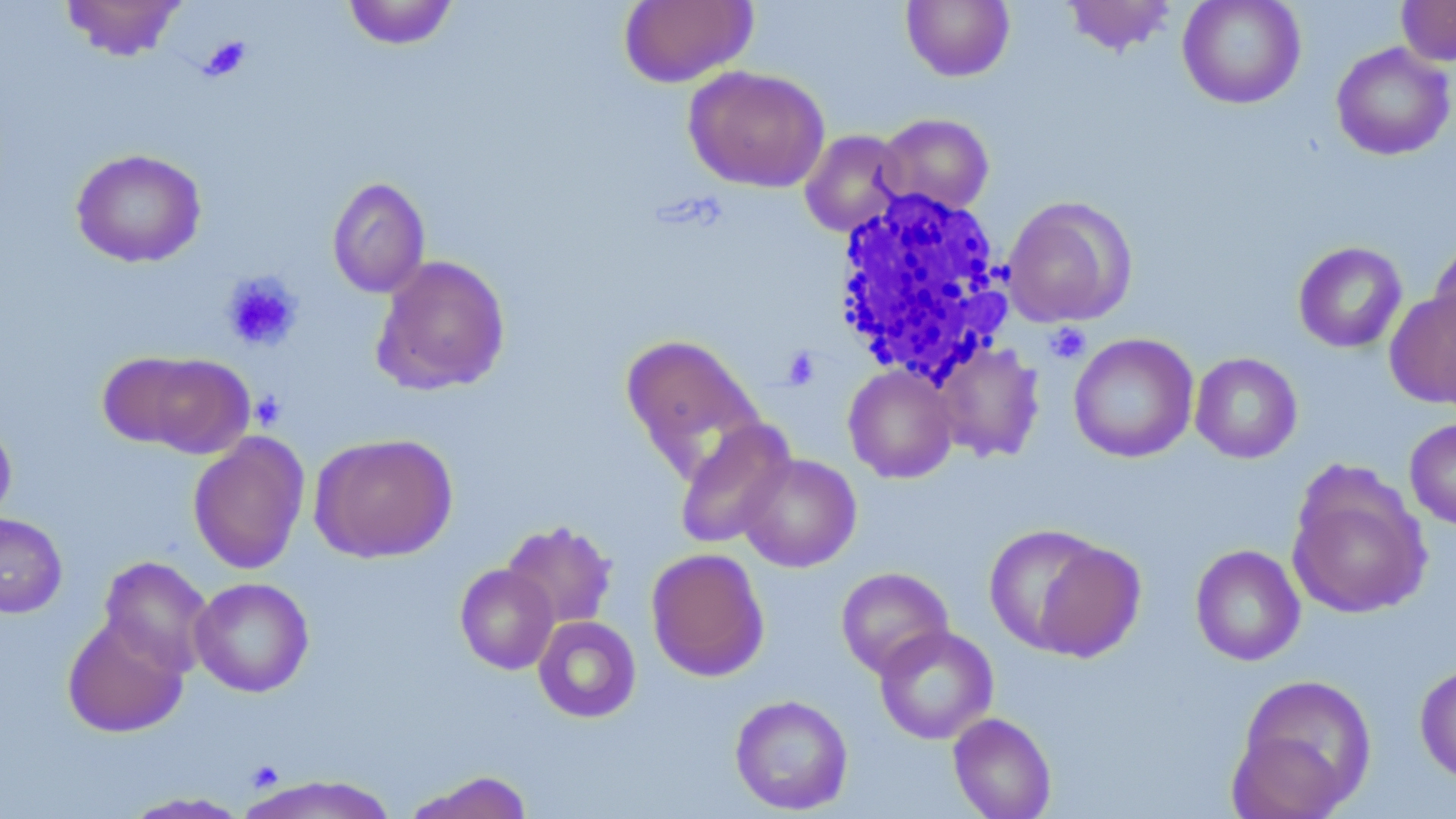

slide-level diagnosis = negative for blood parasites
image size = 1456×819 pixels
modality = light microscopy
magnification = 1000x
uninfected red blood cell locations = approximate bounding boxes as [x1, y1, x2, y2] in pixels: [59, 0, 187, 61], [342, 0, 459, 50], [619, 0, 758, 87], [901, 0, 1015, 82], [1062, 0, 1178, 56], [1177, 0, 1306, 109], [1396, 0, 1456, 67], [1331, 42, 1455, 161], [683, 65, 830, 193], [877, 113, 994, 216], [799, 129, 908, 237], [70, 148, 207, 268], [327, 176, 430, 298], [1002, 196, 1137, 328], [1428, 237, 1456, 358], [1293, 241, 1407, 353], [371, 254, 511, 396], [1385, 291, 1456, 408], [619, 333, 766, 479], [1068, 333, 1199, 463], [934, 340, 1045, 462], [109, 350, 256, 457], [1190, 352, 1303, 463], [843, 365, 959, 483], [0, 416, 17, 527], [674, 418, 796, 550], [1404, 418, 1456, 530], [188, 432, 309, 575], [309, 432, 458, 564], [737, 453, 862, 572], [1286, 471, 1432, 619], [0, 511, 68, 618], [500, 520, 618, 630], [983, 524, 1111, 654], [1027, 539, 1146, 662], [1190, 543, 1306, 666], [645, 548, 769, 682], [99, 556, 214, 676], [454, 563, 559, 675], [836, 566, 953, 678], [189, 577, 314, 697], [62, 615, 188, 737], [533, 616, 641, 723], [874, 625, 998, 744], [1414, 662, 1456, 784], [1233, 673, 1377, 815], [729, 694, 854, 815], [948, 712, 1056, 819], [403, 771, 534, 819], [243, 775, 399, 818], [120, 792, 251, 818]
stain = May-Grünwald-Giemsa
white blood cell locations = approximate bounding boxes as [x1, y1, x2, y2] in pixels: [830, 186, 1016, 386]
platelet locations = approximate bounding boxes as [x1, y1, x2, y2] in pixels: [199, 36, 252, 81], [220, 272, 303, 352], [1045, 323, 1091, 364], [781, 346, 821, 391], [250, 390, 286, 430], [246, 760, 284, 792]
preparation = thin blood film
field of view = one of a larger specimen